Comment on the morphology of the red blood cells.
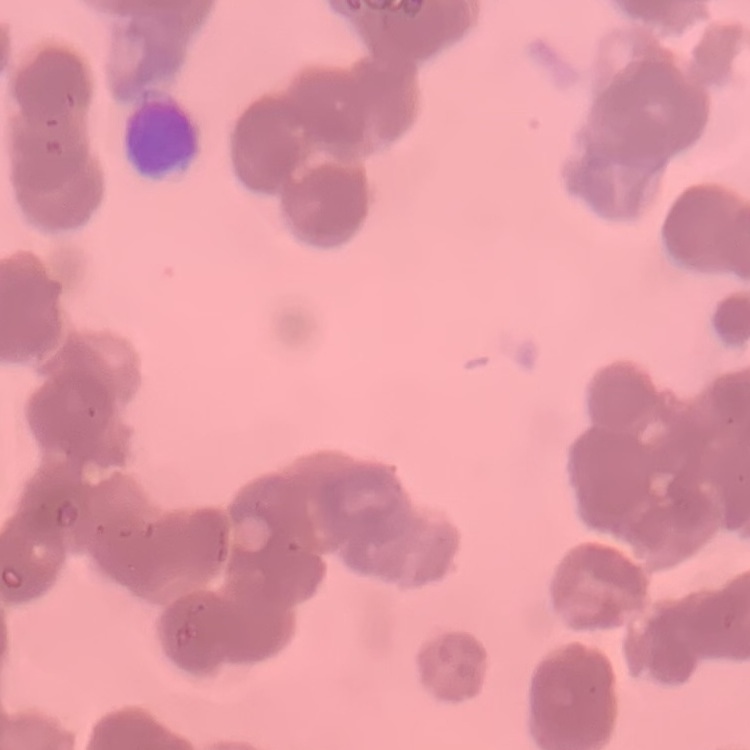
They show rouleaux formation.

{
  "stain": "Field's or Giemsa",
  "image_type": "square crop of a larger photomicrograph",
  "preparation": "thin blood smear"
}